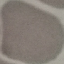
Result: negative for malaria parasites. Giemsa stain. Thin smear of blood. Cell patch, automatically extracted from a larger field of view and resized to 64 × 64 pixels. Acquired by smartphone through the microscope eyepiece.